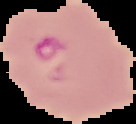

Summary:
  - Image size: 136×124 pixels
  - Image type: segmented cell region on a black background
  - Malaria status: parasitized
  - Preparation: thin blood smear